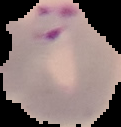 From a thin blood film. Malaria status: parasitized. Image is 121×127 pixels. Cell region segmented out of the field of view; the surrounding area is masked to black.